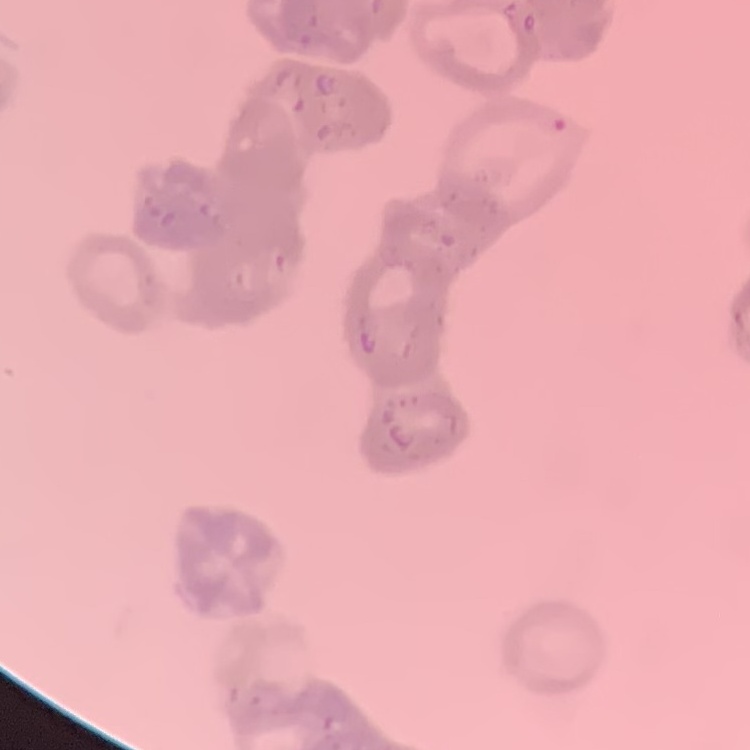

{
  "red_blood_cell_morphology": "rouleaux formation",
  "stain": "Field's or Giemsa",
  "image_type": "one tile cut from a larger photomicrograph",
  "preparation": "thin blood film"
}